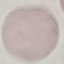

Summary:
  - Result: negative for malaria parasites
  - Image type: automatically extracted cell patch, resized to 64 × 64 pixels
  - Preparation: thin smear
  - Capture: smartphone through the microscope eyepiece
  - Stain: Giemsa